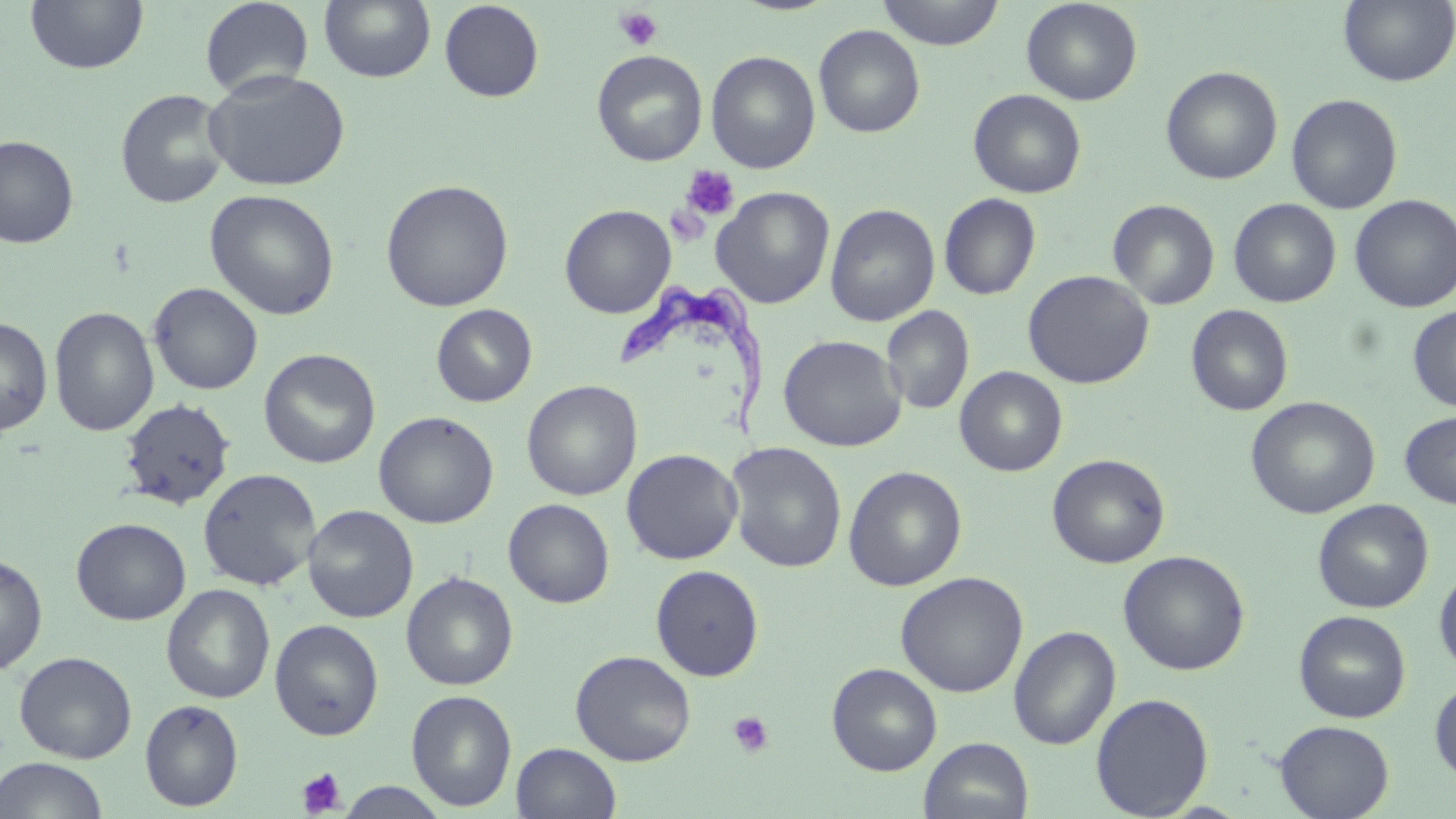

Trypanosoma brucei locations = approximate bounding boxes as (x1,y1)-(x2,y2) corner pairs in pixels: (616,281)-(769,442)
slide-level diagnosis = Trypanosoma brucei
preparation = thin blood smear
platelet locations = approximate bounding boxes as (x1,y1)-(x2,y2) corner pairs in pixels: (613,6)-(663,52), (680,164)-(740,222), (665,205)-(711,248), (727,711)-(775,756), (297,767)-(346,816)
magnification = 1000x
stain = May-Grünwald-Giemsa
image size = 1456×819 pixels
uninfected red blood cell locations = approximate bounding boxes as (x1,y1)-(x2,y2) corner pairs in pixels: (24,0)-(149,75), (199,0)-(315,99), (318,0)-(436,84), (439,0)-(544,103), (877,0)-(1005,50), (1020,0)-(1143,105), (1338,0)-(1455,87), (813,25)-(926,138), (591,50)-(708,166), (705,50)-(820,174), (1160,66)-(1283,185), (203,70)-(350,192), (115,88)-(230,209), (967,89)-(1087,198), (1286,93)-(1402,214), (0,135)-(79,249), (380,179)-(514,312), (711,187)-(835,308), (204,189)-(340,320), (939,193)-(1041,300), (1349,194)-(1456,313), (1229,198)-(1342,307), (1107,199)-(1220,310), (559,204)-(676,319), (825,204)-(940,326), (1022,270)-(1154,389), (149,282)-(263,395), (431,304)-(537,406), (1186,304)-(1294,416), (49,305)-(159,437), (881,306)-(974,415), (1408,306)-(1456,412), (0,316)-(53,436), (778,334)-(906,452), (259,349)-(381,469), (955,366)-(1068,476), (522,379)-(642,501), (1245,396)-(1380,519), (119,398)-(235,510), (1399,410)-(1456,509), (374,411)-(498,529), (724,441)-(847,573), (621,448)-(743,565), (1047,453)-(1170,568), (843,465)-(967,591), (197,468)-(321,590), (503,498)-(615,608), (1313,499)-(1433,613), (302,505)-(418,623), (71,518)-(191,625), (1118,550)-(1250,675), (0,553)-(48,675), (650,564)-(765,681), (1434,566)-(1456,677), (401,571)-(518,691), (895,571)-(1029,697), (161,583)-(275,704), (1294,610)-(1411,723), (269,619)-(384,741), (1008,625)-(1121,750), (570,650)-(697,765), (14,651)-(137,763), (827,663)-(942,776), (1429,680)-(1456,785), (406,689)-(518,811), (1090,693)-(1214,818), (140,699)-(244,811), (1274,720)-(1394,819), (919,737)-(1034,819), (511,742)-(622,819), (0,757)-(109,819), (336,780)-(451,818)
modality = optical microscopy
field of view = one of a larger specimen